Assess the morphology of the erythrocytes.
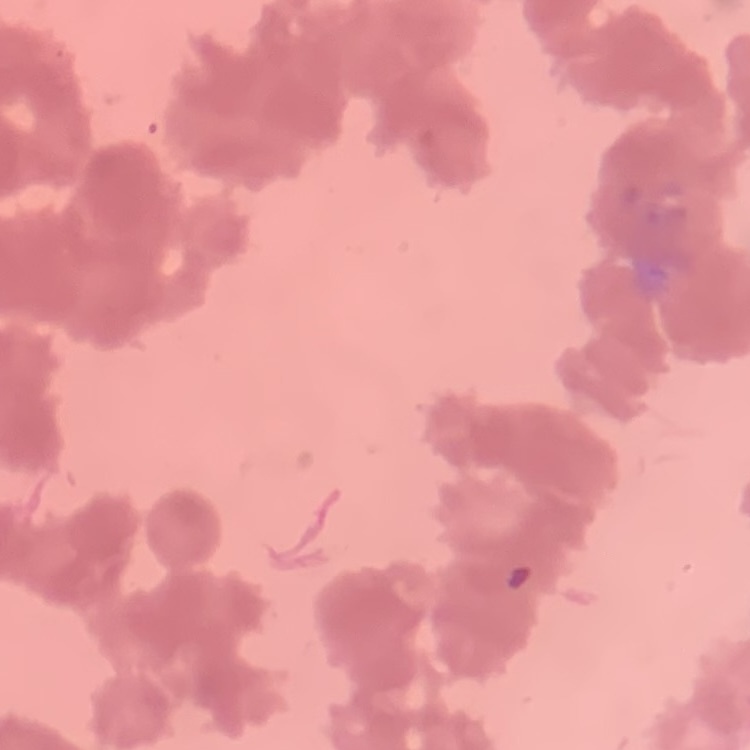
Rouleaux formation.

Summary:
  - Image type: square crop of a larger photomicrograph
  - Preparation: thin peripheral smear
  - Stain: Field's or Giemsa